Report the malaria status of this cell.
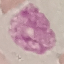
It is uninfected.

Giemsa-stained preparation. Thin blood smear. Acquired by smartphone through the microscope eyepiece. Cell patch, automatically extracted from a larger field of view and resized to 64 × 64 pixels.